Assess the morphology of the red blood cells.
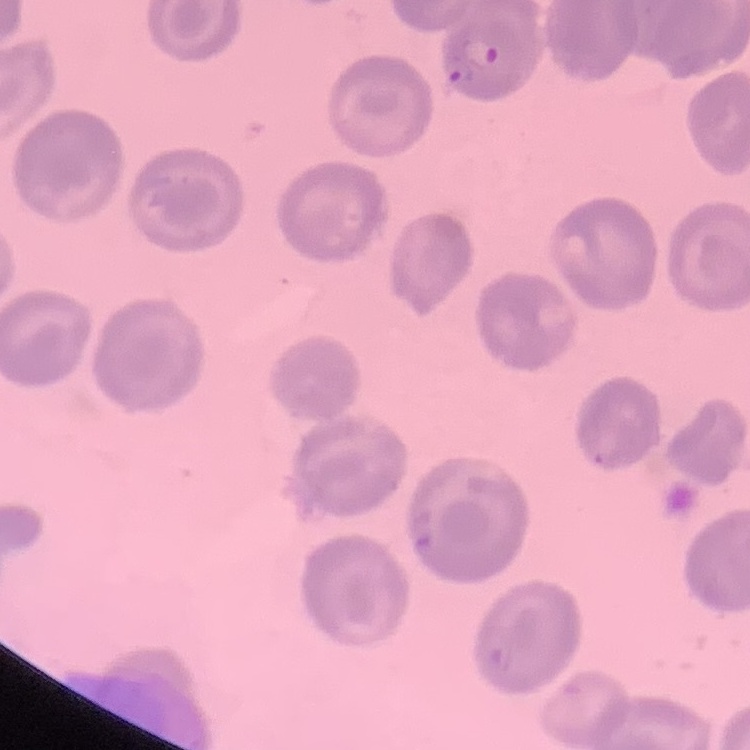

They show no rouleaux formation.

Summary:
  - Stain: Field's or Giemsa
  - Image type: square crop of a larger photomicrograph
  - Preparation: thin blood smear